Report the malaria status of this cell.
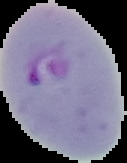

Parasitized.

The area outside the segmented cell region is set to black. Image is 127×163 pixels. From a thin blood film.